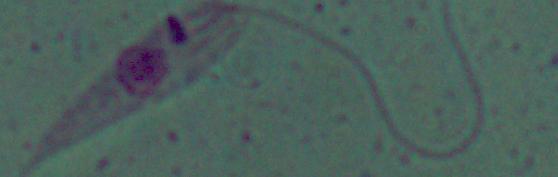
1000x magnification. Photomicrograph. A Leishmania parasite is shown.